Outline each blood parasite and name the species.
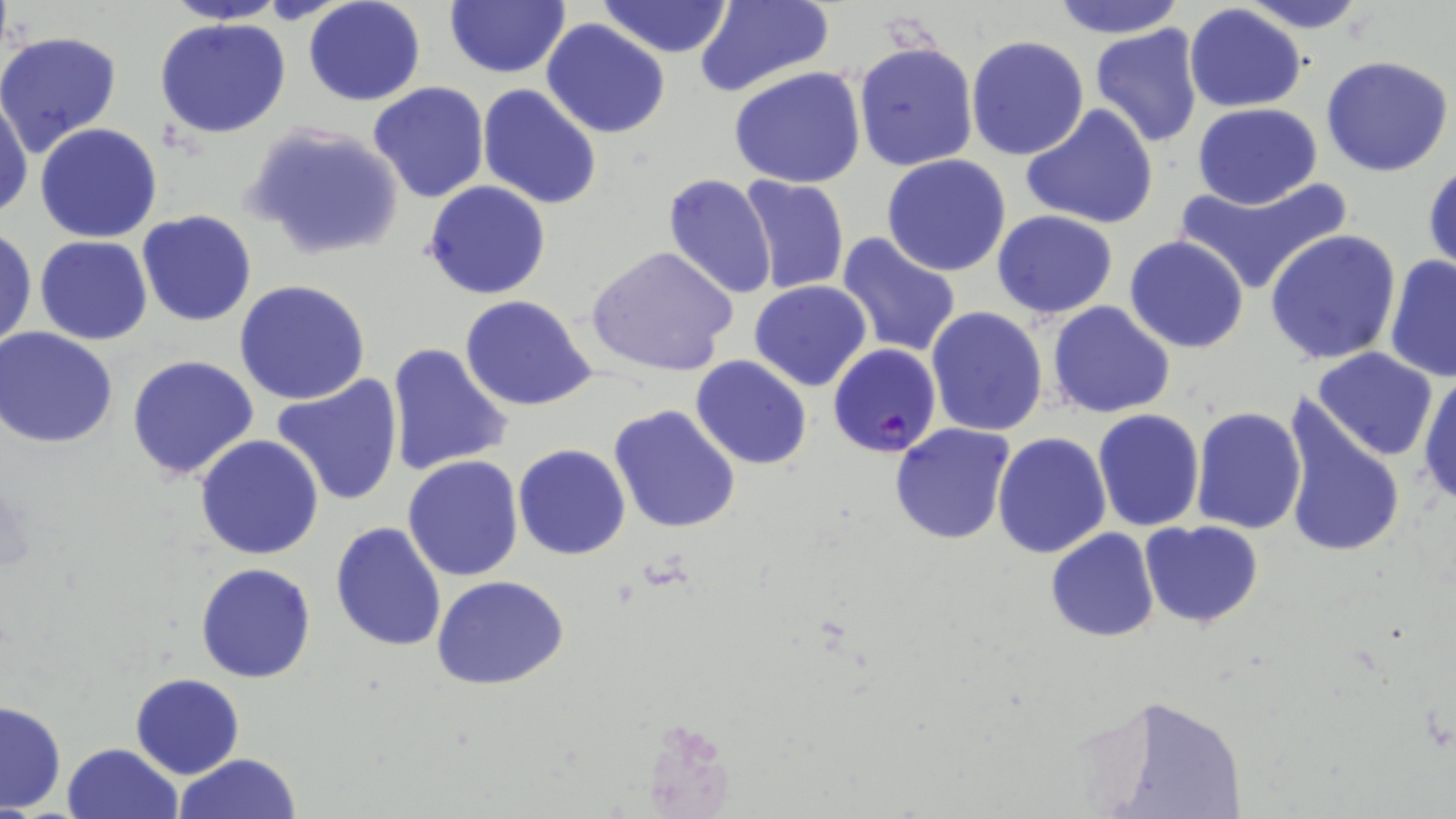

Approximate bounding boxes as (x1,y1)-(x2,y2) corner pairs in pixels.
Plasmodium falciparum-infected red blood cells: (828,343)-(941,459).
No Plasmodium ovale, Plasmodium malariae, Plasmodium vivax, Babesia divergens, or Trypanosoma brucei observed.

{
  "slide_level_diagnosis": "Plasmodium falciparum",
  "image_size": "1456×819 pixels",
  "magnification": "1000x",
  "uninfected_red_blood_cell_locations": "approximate bounding boxes as (x1,y1)-(x2,y2) corner pairs in pixels: (302,0)-(426,107), (444,0)-(569,78), (595,0)-(733,59), (694,0)-(834,99), (1053,0)-(1184,38), (1238,0)-(1374,31), (162,1)-(292,25), (1183,4)-(1308,112), (153,16)-(294,139), (542,19)-(670,139), (1090,22)-(1204,148), (0,29)-(121,153), (966,34)-(1090,159), (853,41)-(978,171), (1320,54)-(1454,177), (729,66)-(867,189), (368,81)-(491,203), (477,83)-(603,211), (0,88)-(33,222), (1192,102)-(1322,209), (1020,104)-(1159,230), (35,122)-(163,242), (243,123)-(405,261), (881,154)-(1013,276), (1424,161)-(1456,275), (663,172)-(778,298), (738,175)-(851,295), (1175,175)-(1352,296), (423,181)-(550,300), (136,211)-(258,327), (990,212)-(1116,320), (0,225)-(36,354), (1264,229)-(1402,365), (835,232)-(961,358), (34,235)-(154,345), (1124,235)-(1251,353), (586,246)-(739,376), (1383,255)-(1456,382), (233,279)-(372,406), (748,279)-(873,391), (460,293)-(598,412), (1048,301)-(1176,418), (925,306)-(1049,437), (0,328)-(120,448), (385,342)-(513,479), (1311,346)-(1440,460), (127,354)-(260,482), (690,355)-(812,470), (1417,365)-(1456,509), (270,374)-(405,507), (1279,396)-(1406,562), (610,404)-(742,534), (1189,405)-(1307,535), (1093,409)-(1205,531), (889,422)-(1017,547), (992,432)-(1110,558), (194,434)-(325,560), (514,443)-(631,561), (401,454)-(524,581), (1139,519)-(1265,630), (329,521)-(448,651), (1045,528)-(1159,642), (194,562)-(317,683), (431,575)-(570,691), (132,673)-(245,778), (1,700)-(67,814), (62,743)-(180,819), (173,752)-(303,819)",
  "preparation": "thin blood smear",
  "modality": "optical microscopy",
  "field_of_view": "one of a larger specimen",
  "stain": "May-Grünwald-Giemsa"
}